Assess this cell for malaria.
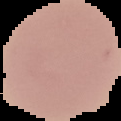

It is uninfected.

{
  "image_size": "121×121 pixels",
  "image_type": "cell region segmented out of the field of view; surrounding area masked to black",
  "preparation": "thin blood film"
}